Point out each Plasmodium parasite.
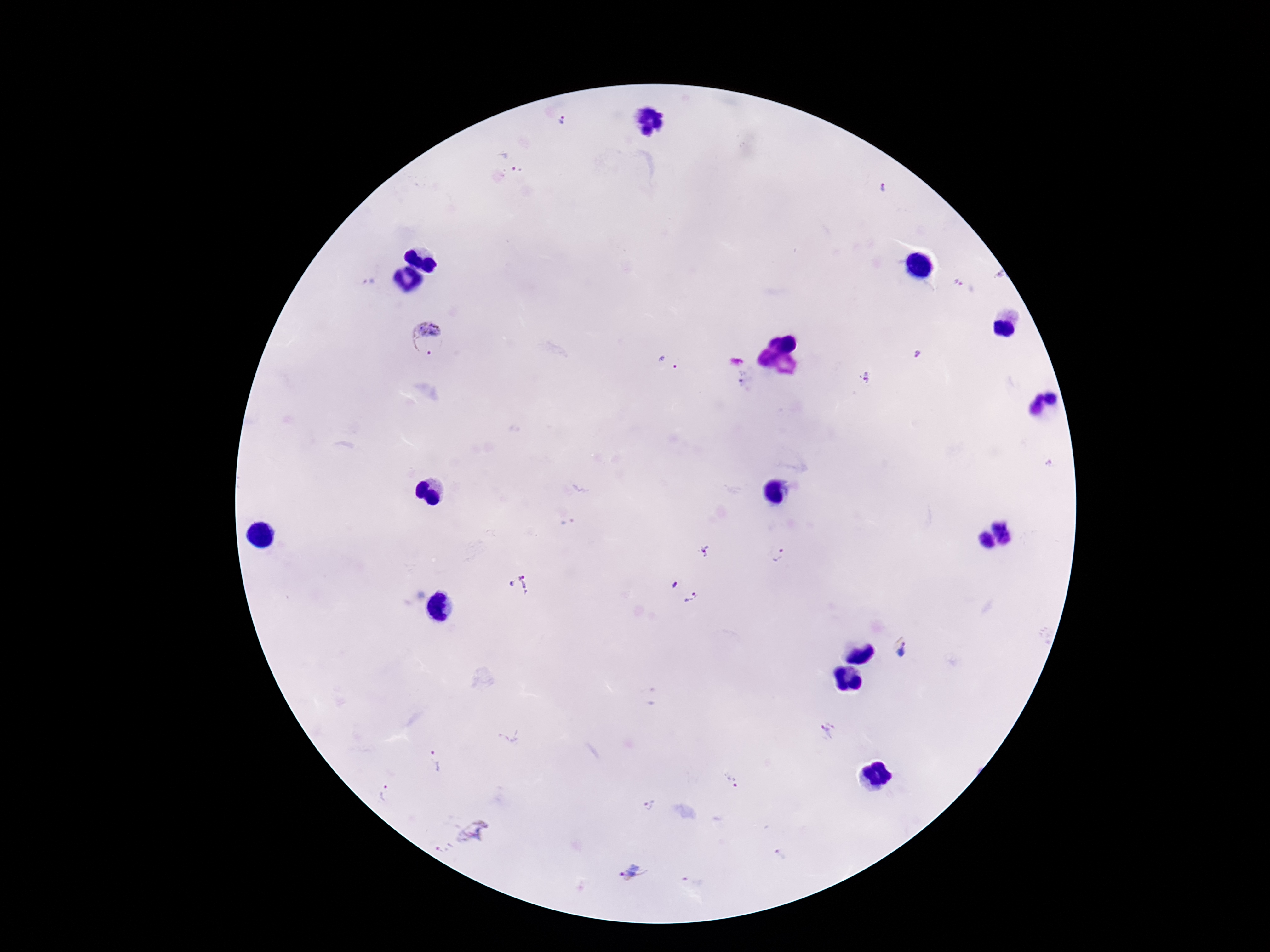
Approximate object centers, in pixels from the top-left corner.
Plasmodium parasites: (x=565, y=121), (x=509, y=162), (x=369, y=283), (x=958, y=283), (x=428, y=340), (x=917, y=354), (x=669, y=363), (x=865, y=378), (x=1049, y=464), (x=707, y=552), (x=776, y=556), (x=521, y=586), (x=682, y=592), (x=903, y=649), (x=827, y=731), (x=435, y=761), (x=732, y=781), (x=386, y=793), (x=649, y=806), (x=473, y=832), (x=779, y=854), (x=632, y=874).

Single field of view. 100x magnification. Giemsa-stained preparation. Thick blood smear. Patient malaria status: infected. Image is 1270×952 pixels. Smartphone photograph taken through the microscope eyepiece.